Assess the morphology of the red blood cells.
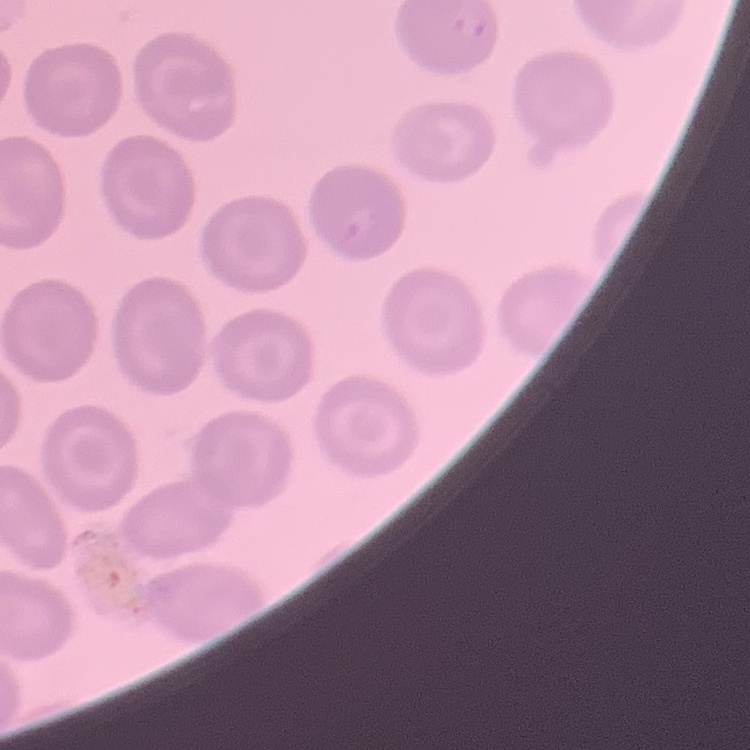

They show no rouleaux formation.

Thin blood smear. Stained with either Field's or Giemsa. Square crop of a larger photomicrograph.